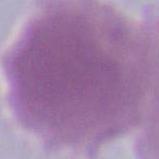

Photomicrograph. Captured at 1000x magnification. An erythrocyte is seen.